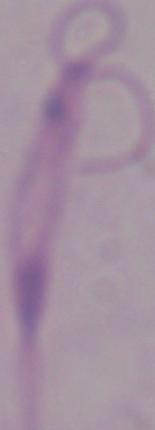
Summary:
  - Identification: Leishmania
  - Modality: photomicrograph
  - Magnification: 1000x